Identify the blood parasite species.
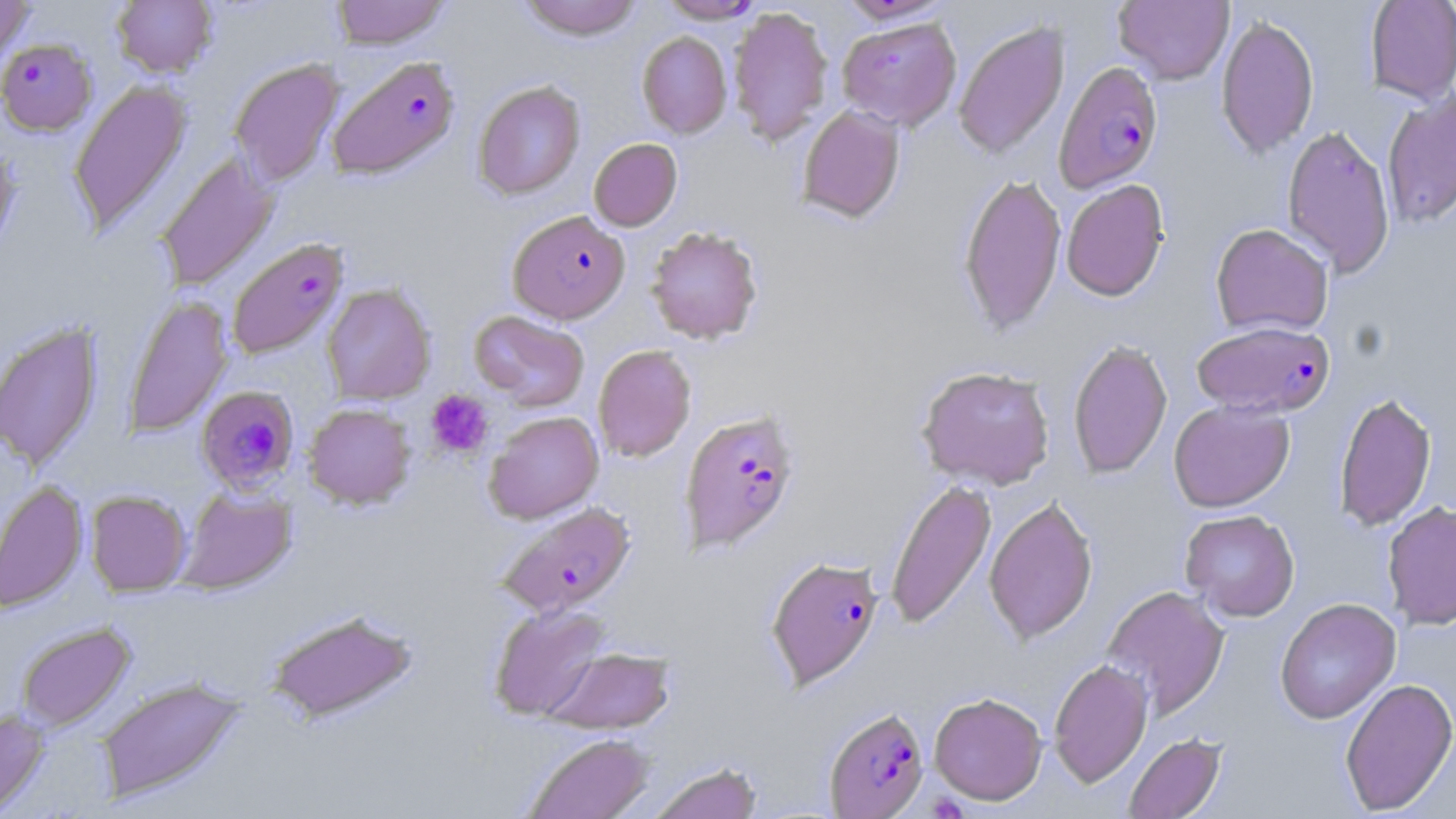

Plasmodium falciparum.

Approximate bounding boxes as named x1/y1/x2/y2 corners in pixels. Uninfected red blood cell locations: (x1=0, y1=0, x2=36, y2=72), (x1=112, y1=0, x2=217, y2=78), (x1=331, y1=0, x2=450, y2=49), (x1=519, y1=0, x2=642, y2=40), (x1=657, y1=0, x2=767, y2=23), (x1=837, y1=0, x2=956, y2=25), (x1=1113, y1=0, x2=1234, y2=85), (x1=1365, y1=0, x2=1456, y2=104), (x1=727, y1=6, x2=834, y2=145), (x1=1216, y1=13, x2=1319, y2=159), (x1=837, y1=16, x2=961, y2=131), (x1=953, y1=20, x2=1070, y2=160), (x1=637, y1=31, x2=732, y2=138), (x1=229, y1=58, x2=344, y2=187), (x1=69, y1=78, x2=193, y2=238), (x1=473, y1=80, x2=585, y2=200), (x1=1381, y1=90, x2=1456, y2=228), (x1=797, y1=105, x2=906, y2=223), (x1=1282, y1=124, x2=1396, y2=277), (x1=589, y1=138, x2=682, y2=231), (x1=0, y1=140, x2=20, y2=263), (x1=155, y1=153, x2=279, y2=291), (x1=958, y1=172, x2=1066, y2=335), (x1=1061, y1=179, x2=1169, y2=301), (x1=1210, y1=223, x2=1333, y2=336), (x1=646, y1=226, x2=763, y2=344), (x1=322, y1=283, x2=436, y2=405), (x1=123, y1=295, x2=233, y2=437), (x1=470, y1=310, x2=589, y2=411), (x1=0, y1=319, x2=104, y2=473), (x1=1068, y1=339, x2=1172, y2=479), (x1=593, y1=344, x2=696, y2=462), (x1=916, y1=365, x2=1055, y2=489), (x1=1333, y1=390, x2=1437, y2=532), (x1=1168, y1=399, x2=1295, y2=512), (x1=303, y1=403, x2=415, y2=509), (x1=484, y1=411, x2=604, y2=523), (x1=885, y1=478, x2=996, y2=630), (x1=0, y1=480, x2=88, y2=613), (x1=177, y1=485, x2=297, y2=595), (x1=86, y1=490, x2=191, y2=596), (x1=984, y1=495, x2=1098, y2=644), (x1=1382, y1=501, x2=1456, y2=630), (x1=1180, y1=510, x2=1300, y2=621), (x1=1102, y1=585, x2=1229, y2=718), (x1=1275, y1=598, x2=1401, y2=724), (x1=488, y1=602, x2=612, y2=722), (x1=266, y1=609, x2=417, y2=723), (x1=15, y1=622, x2=136, y2=732), (x1=544, y1=647, x2=674, y2=734), (x1=1048, y1=658, x2=1153, y2=788), (x1=95, y1=676, x2=248, y2=804), (x1=1339, y1=677, x2=1456, y2=815), (x1=929, y1=692, x2=1047, y2=804), (x1=0, y1=709, x2=50, y2=816), (x1=522, y1=732, x2=655, y2=819), (x1=1123, y1=732, x2=1226, y2=819), (x1=647, y1=761, x2=763, y2=819). Platelet locations: (x1=425, y1=390, x2=493, y2=458), (x1=924, y1=788, x2=971, y2=819). Plasmodium falciparum-infected red blood cell locations: (x1=0, y1=38, x2=97, y2=136), (x1=327, y1=55, x2=460, y2=180), (x1=1053, y1=60, x2=1164, y2=193), (x1=507, y1=211, x2=630, y2=324), (x1=227, y1=237, x2=348, y2=359), (x1=1192, y1=320, x2=1334, y2=418), (x1=197, y1=385, x2=299, y2=493), (x1=679, y1=408, x2=801, y2=554), (x1=497, y1=502, x2=636, y2=617), (x1=766, y1=556, x2=884, y2=689), (x1=824, y1=706, x2=928, y2=818). Captured at 1000x magnification. Optical microscopy. Single field of view. Thin blood film. Image is 1456×819 pixels. May-Grünwald-Giemsa-stained preparation.